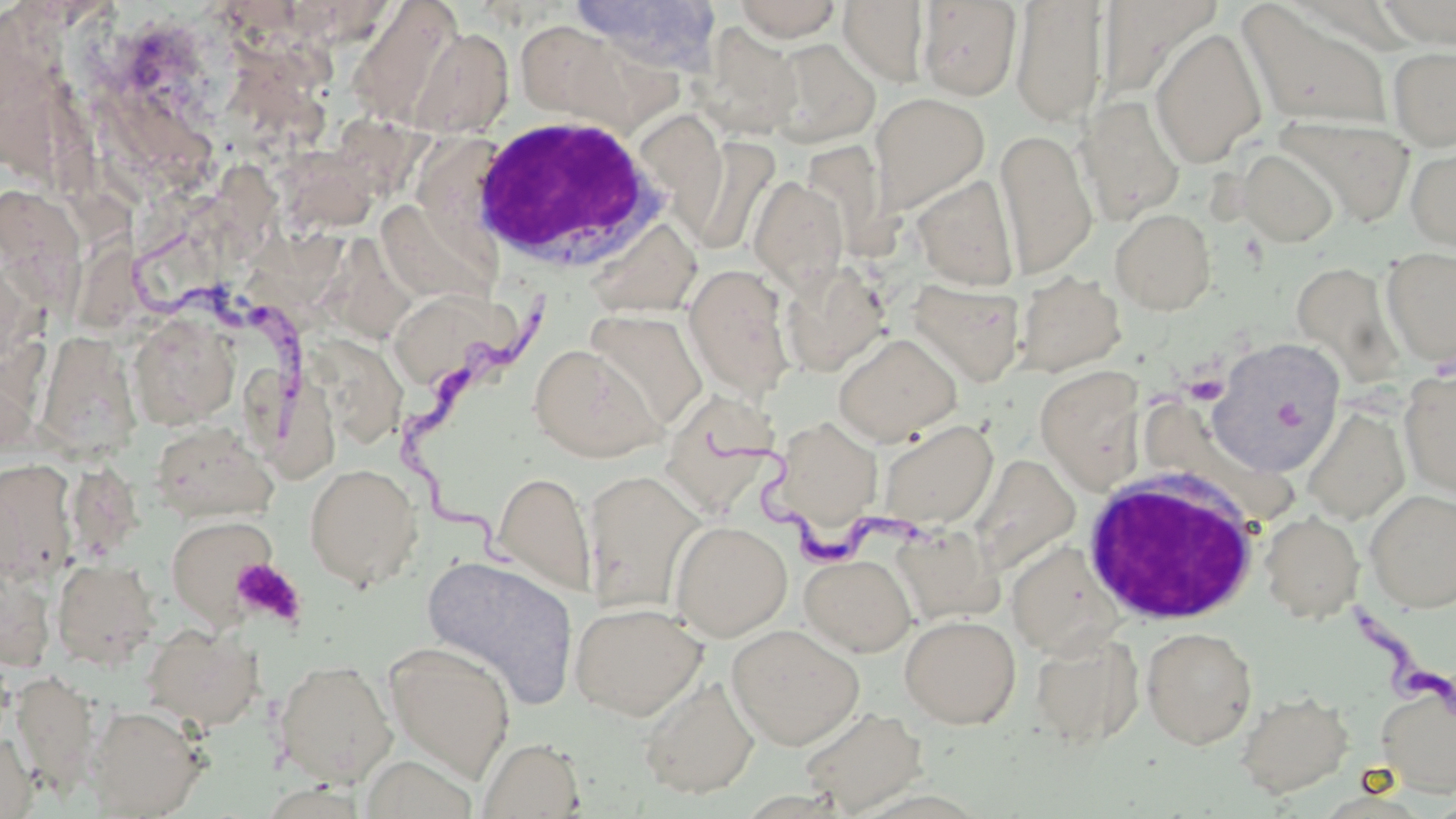

{
  "slide_level_diagnosis": "Trypanosoma brucei",
  "uninfected_red_blood_cell_locations": "approximate bounding boxes as (x1, y1, x2, y2) in pixels: (572, 0, 726, 76), (732, 0, 844, 41), (838, 0, 930, 86), (1096, 0, 1221, 104), (1377, 0, 1456, 47), (916, 1, 1022, 101), (1010, 2, 1108, 127), (1237, 2, 1394, 131), (347, 3, 461, 127), (514, 17, 628, 122), (697, 23, 803, 140), (406, 26, 515, 138), (1150, 26, 1267, 168), (766, 38, 881, 147), (1387, 45, 1456, 150), (870, 92, 990, 215), (1076, 95, 1186, 224), (1276, 115, 1415, 226), (995, 128, 1097, 278), (681, 137, 780, 256), (1405, 141, 1456, 251), (1237, 148, 1339, 247), (272, 149, 378, 238), (912, 175, 1020, 291), (749, 176, 848, 292), (0, 185, 100, 330), (377, 199, 497, 308), (1110, 208, 1217, 314), (586, 218, 702, 317), (315, 226, 425, 349), (1381, 248, 1456, 367), (778, 261, 892, 376), (1291, 262, 1405, 388), (684, 263, 796, 400), (1014, 272, 1126, 376), (908, 279, 1026, 386), (393, 298, 517, 384), (583, 309, 707, 434), (128, 312, 238, 429), (310, 320, 409, 446), (46, 329, 141, 459), (833, 332, 962, 445), (1210, 339, 1345, 475), (528, 343, 663, 462), (1035, 365, 1145, 490), (247, 366, 346, 478), (1399, 369, 1456, 497), (665, 396, 780, 511), (1302, 407, 1410, 525), (770, 417, 884, 533), (877, 419, 998, 529), (150, 421, 277, 523), (972, 454, 1080, 574), (0, 458, 79, 585), (304, 462, 423, 591), (584, 468, 705, 613), (493, 470, 596, 596), (1365, 489, 1456, 612), (1260, 511, 1364, 622), (165, 514, 278, 627), (670, 519, 792, 641), (891, 525, 1002, 625), (1006, 541, 1122, 657), (800, 553, 916, 656), (420, 555, 579, 706), (51, 558, 161, 669), (569, 601, 708, 720), (900, 614, 1021, 727), (141, 623, 264, 731), (727, 623, 864, 749), (1141, 626, 1257, 749), (1030, 631, 1146, 748), (384, 642, 515, 782), (273, 659, 398, 786), (10, 669, 101, 795), (639, 676, 760, 798), (1375, 683, 1456, 798), (1235, 690, 1354, 798), (87, 705, 208, 817), (798, 705, 930, 815), (0, 730, 36, 819), (478, 737, 586, 818), (360, 755, 480, 819)",
  "platelet_locations": "approximate bounding boxes as (x1, y1, x2, y2) in pixels: (1184, 375, 1228, 405), (230, 557, 306, 628)",
  "trypanosoma_brucei_locations": "approximate bounding boxes as (x1, y1, x2, y2) in pixels: (130, 232, 324, 440), (412, 296, 551, 582), (700, 424, 925, 581), (1346, 599, 1456, 718)",
  "field_of_view": "one of a larger specimen",
  "magnification": "1000x",
  "stain": "May-Grünwald-Giemsa",
  "preparation": "thin blood smear",
  "modality": "optical microscopy",
  "white_blood_cell_locations": "approximate bounding boxes as (x1, y1, x2, y2) in pixels: (465, 113, 673, 274), (1078, 465, 1263, 626)",
  "image_size": "1456×819 pixels"
}